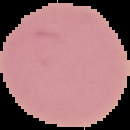

The area outside the segmented cell region is set to black. Image is 130×130 pixels. Malaria status: uninfected. From a thin blood film.